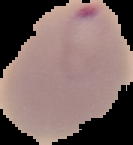
image size = 133×145 pixels
preparation = thin blood film
image type = segmented cell region on a black background
result = Plasmodium parasites identified